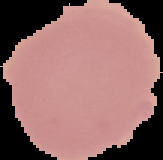

image type = cell region segmented out of the field of view; surrounding area masked to black
preparation = thin blood film
image size = 163×160 pixels
result = no Plasmodium parasites detected